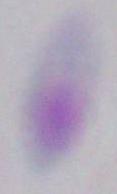

Summary:
  - Identification: Toxoplasma gondii
  - Magnification: 1000x
  - Modality: micrograph